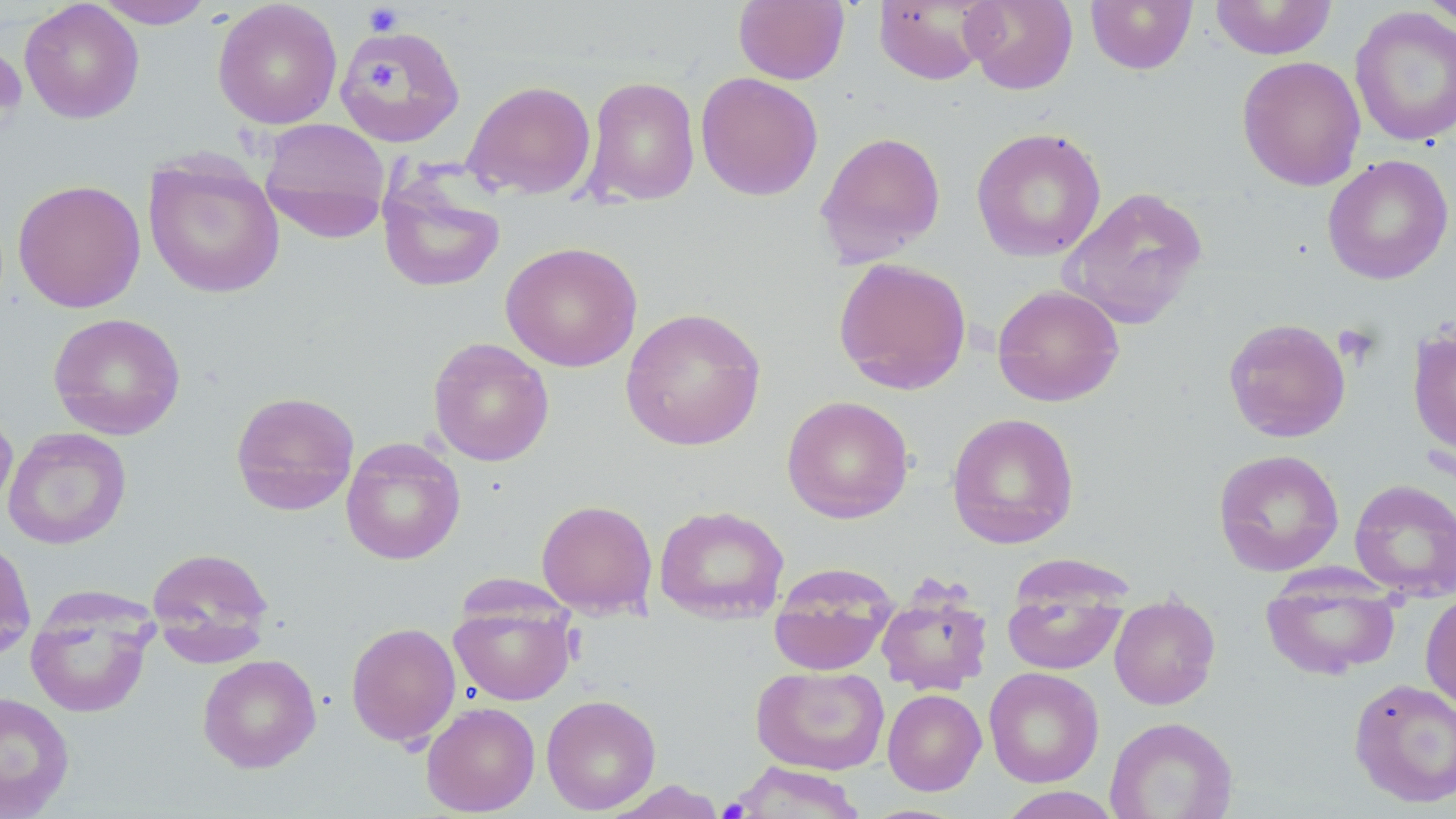
slide-level diagnosis = no evidence of blood parasites
image size = 1456×819 pixels
stain = May-Grünwald-Giemsa
preparation = thin blood film
magnification = 1000x
field of view = one of a larger specimen
uninfected red blood cell locations = approximate bounding boxes as [x1, y1, x2, y2] in pixels: [92, 0, 215, 28], [733, 0, 850, 85], [873, 0, 995, 85], [961, 0, 1078, 95], [1086, 0, 1197, 74], [1419, 0, 1456, 29], [19, 1, 144, 124], [212, 1, 343, 129], [1210, 1, 1336, 60], [1349, 6, 1456, 147], [334, 25, 466, 147], [1236, 55, 1365, 191], [695, 71, 823, 201], [583, 76, 701, 207], [463, 80, 597, 200], [258, 118, 393, 241], [971, 127, 1107, 262], [815, 130, 946, 266], [142, 154, 285, 298], [1322, 154, 1454, 286], [378, 174, 505, 293], [12, 178, 146, 313], [1059, 186, 1208, 330], [500, 242, 642, 372], [832, 257, 972, 396], [992, 284, 1125, 406], [620, 307, 767, 451], [48, 312, 186, 440], [1223, 317, 1351, 443], [1407, 327, 1456, 457], [428, 337, 555, 466], [230, 390, 360, 516], [782, 395, 914, 524], [0, 403, 18, 517], [946, 412, 1079, 549], [3, 427, 131, 550], [341, 437, 465, 565], [1213, 448, 1345, 576], [1350, 478, 1456, 601], [536, 499, 658, 618], [653, 505, 790, 624], [0, 534, 36, 663], [146, 546, 274, 662], [768, 563, 899, 676], [1261, 568, 1400, 680], [1002, 575, 1129, 676], [876, 586, 993, 696], [24, 588, 159, 718], [1420, 591, 1456, 711], [449, 593, 577, 706], [1109, 594, 1220, 710], [346, 622, 461, 747], [197, 653, 321, 772], [751, 664, 890, 776], [984, 667, 1104, 787], [1348, 677, 1456, 809], [882, 688, 986, 795], [0, 691, 75, 817], [541, 694, 661, 814], [421, 701, 540, 816], [1105, 716, 1238, 819], [728, 762, 868, 818], [996, 786, 1122, 818]
platelet locations = approximate bounding boxes as [x1, y1, x2, y2] in pixels: [363, 3, 404, 37], [0, 45, 27, 127], [367, 65, 398, 92], [1333, 323, 1381, 367]
modality = optical microscopy